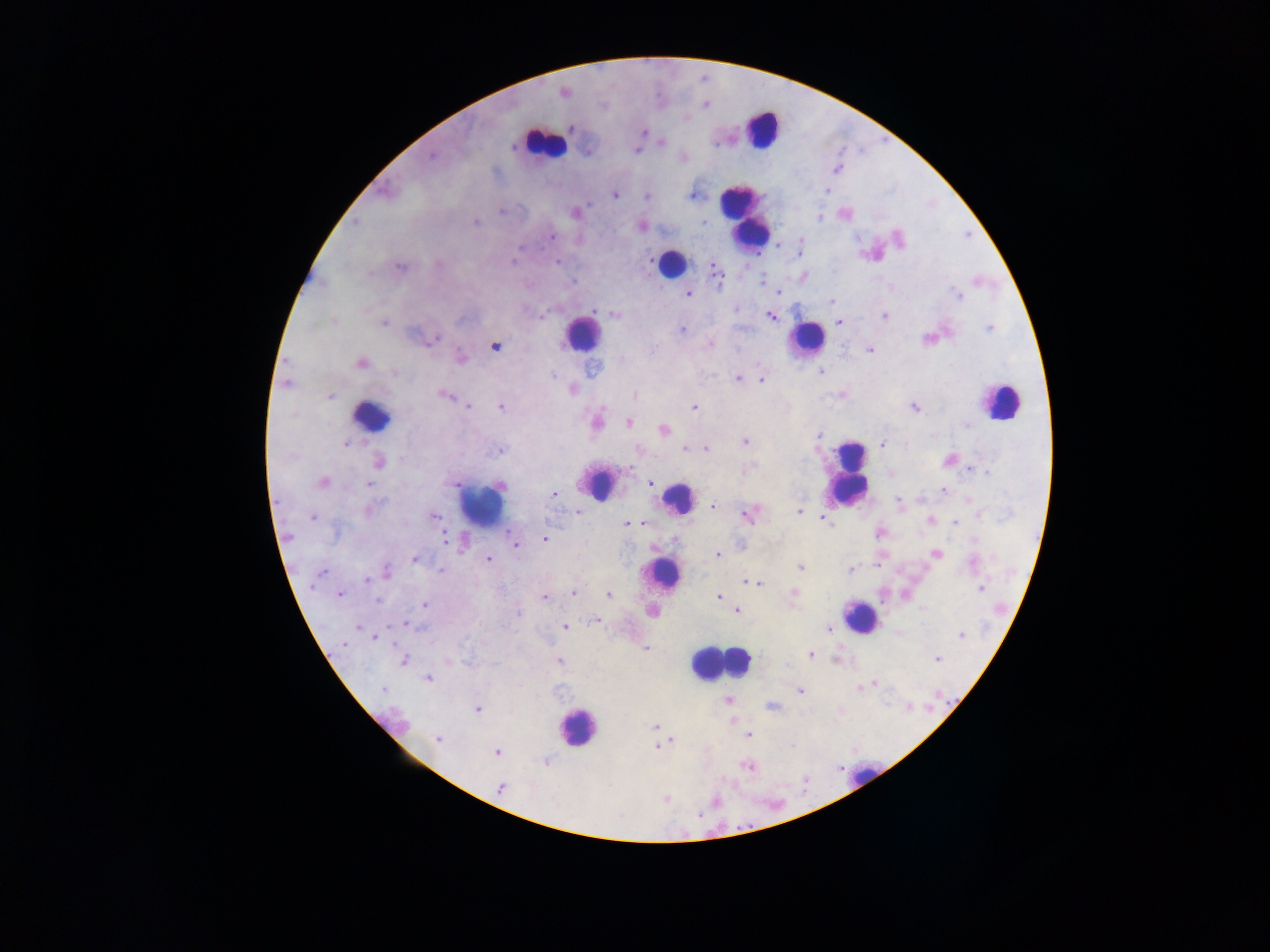

Approximate centers as (x, y) in pixels.
Summary:
  - Malaria parasite locations: (563, 92), (705, 105), (570, 128), (644, 131), (661, 142), (715, 144), (513, 147), (636, 150), (432, 157), (836, 169), (827, 191), (615, 195), (693, 195), (647, 196), (589, 203), (501, 212), (575, 213), (820, 218), (703, 221), (355, 222), (475, 222), (641, 226), (552, 236), (900, 238), (801, 241), (778, 246), (520, 247), (799, 251), (516, 254), (513, 262), (557, 262), (437, 264), (400, 267), (716, 272), (762, 282), (779, 292), (687, 294), (959, 296), (831, 302), (594, 310), (615, 316), (771, 317), (884, 317), (334, 321), (839, 322), (383, 323), (989, 328), (682, 330), (435, 339), (709, 346), (495, 347), (870, 350), (460, 356), (621, 360), (360, 363), (592, 368), (821, 372), (394, 373), (553, 376), (737, 378), (762, 380), (286, 384), (573, 389), (443, 395), (329, 396), (634, 396), (467, 406), (500, 406), (694, 406), (915, 407), (596, 422), (629, 422), (966, 426), (663, 430), (820, 434), (745, 442), (346, 443), (882, 445), (686, 449), (705, 449), (499, 450), (638, 450), (402, 458), (949, 459), (378, 462), (971, 470), (988, 472), (323, 483), (649, 483), (368, 485), (500, 485), (942, 491), (553, 494), (384, 501), (900, 503), (714, 505), (368, 511), (799, 511), (577, 512), (748, 514), (980, 514), (434, 516), (311, 518), (825, 520), (930, 521), (956, 522), (637, 523), (628, 524), (828, 524), (880, 532), (445, 538), (544, 539), (973, 540), (515, 546), (935, 553), (718, 555), (414, 559), (488, 559), (973, 562), (878, 564), (800, 567), (851, 570), (387, 571), (441, 571), (321, 572), (367, 580), (748, 582), (758, 584), (981, 589), (574, 593), (340, 594), (793, 594), (609, 595), (544, 597), (718, 597), (376, 600), (424, 604), (652, 611), (737, 611), (518, 613), (595, 620), (406, 625), (358, 627), (564, 627), (828, 628), (961, 635), (375, 638), (344, 644), (646, 649), (811, 655), (403, 660), (558, 660), (937, 660), (429, 678), (875, 684), (866, 685), (861, 688), (382, 689), (801, 691), (727, 699), (772, 707), (478, 710), (654, 727), (749, 735), (438, 739), (669, 741), (657, 746), (496, 753), (545, 763), (748, 766), (500, 788), (665, 799), (715, 802), (700, 815)
  - Leukocyte locations (subset; some below the resolvable size): (763, 128), (543, 143), (744, 217), (670, 263), (581, 333), (806, 339), (1000, 402), (371, 417), (850, 472), (601, 485), (677, 499), (481, 505), (662, 572), (860, 617), (737, 661), (717, 663), (577, 727), (863, 775)
  - Preparation: thick blood smear
  - Field of view: single
  - Capture: mobile-phone photograph through a microscope
  - Country: Ghana
  - Image size: 1270×952 pixels